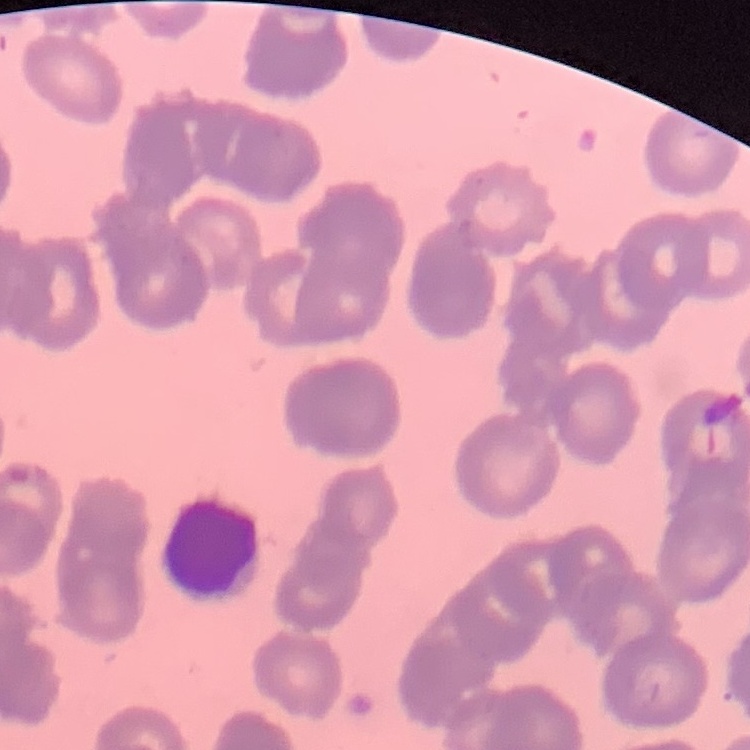
erythrocyte morphology = rouleaux formation
stain = Field's or Giemsa
preparation = thin blood film
image type = one tile cut from a larger photomicrograph